Assess the morphology of the erythrocytes.
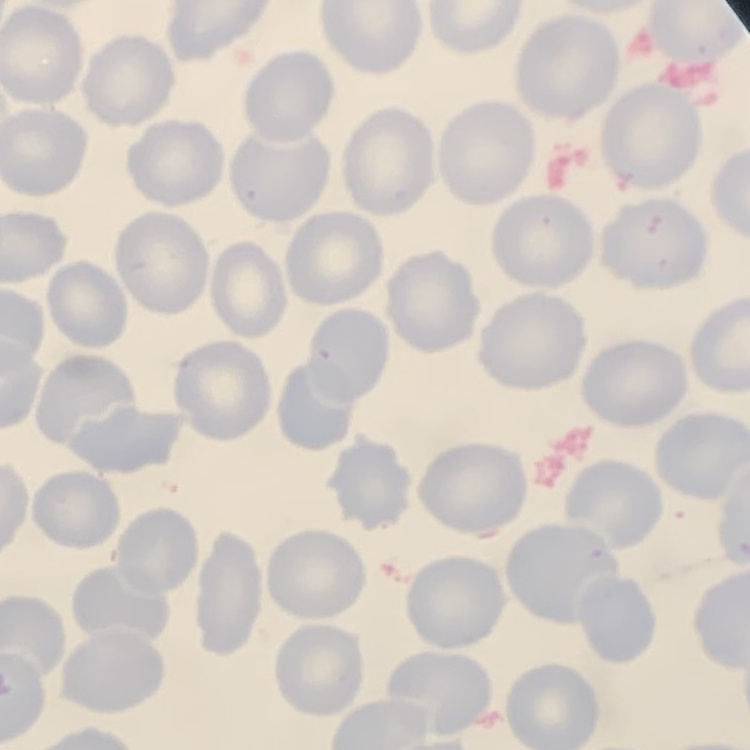

No rouleaux formation.

Summary:
  - Stain: Field's or Giemsa
  - Preparation: thin blood smear
  - Image type: one tile cut from a larger photomicrograph